Locate the cells, classifying each as a parasitized RBC, an uninfected RBC, or a WBC.
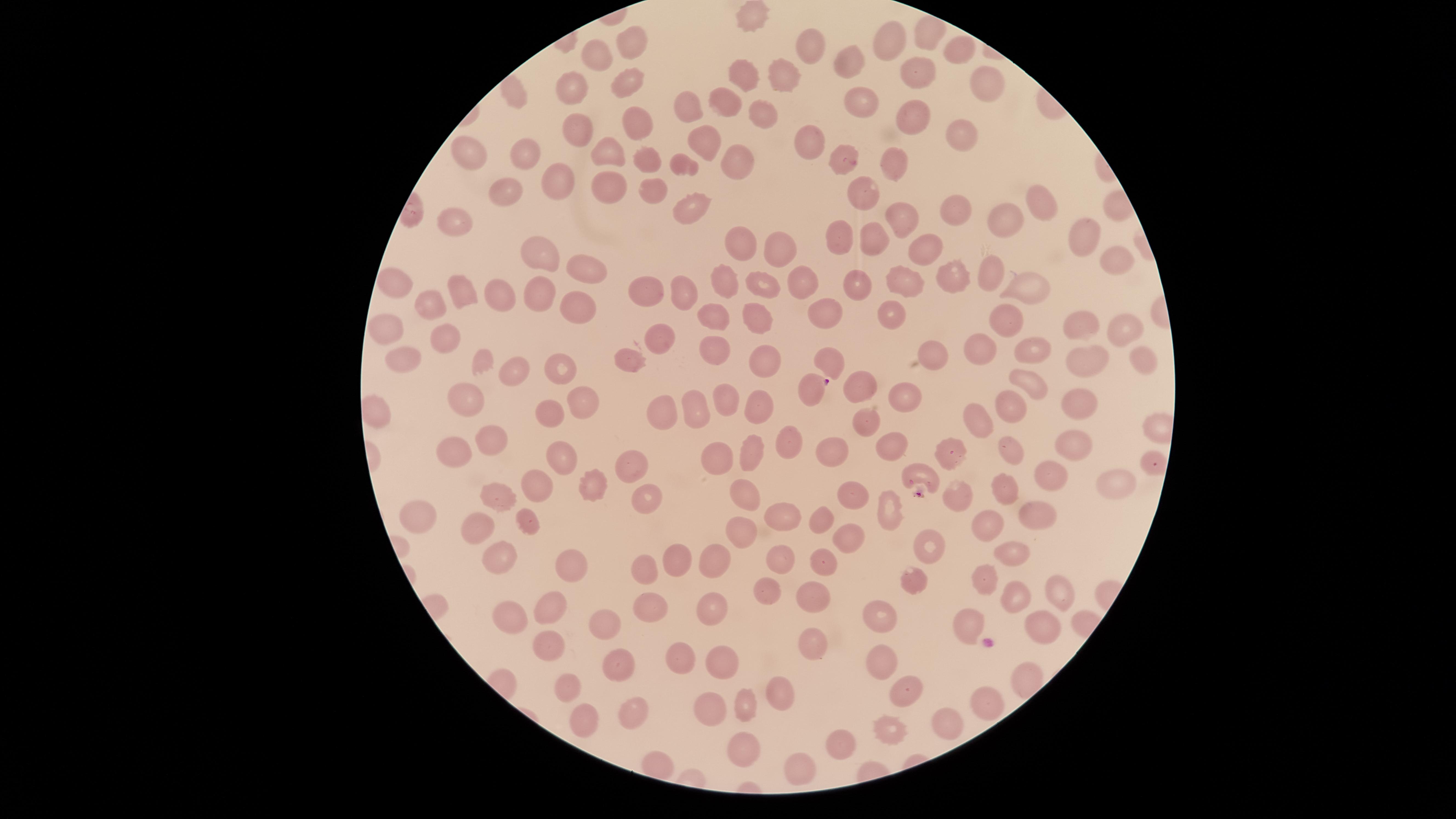
Approximate marker points, in pixels from the top-left corner.
Parasitized RBCs: (x=807, y=392), (x=920, y=477).
Uninfected RBCs: (x=750, y=21), (x=926, y=35), (x=635, y=41), (x=806, y=44), (x=891, y=45), (x=951, y=49), (x=600, y=55), (x=841, y=60), (x=912, y=68), (x=744, y=76), (x=785, y=78), (x=623, y=79), (x=574, y=83), (x=515, y=87), (x=989, y=90), (x=854, y=100), (x=728, y=102), (x=679, y=106), (x=910, y=114), (x=761, y=118), (x=635, y=123), (x=567, y=129), (x=959, y=140), (x=807, y=141), (x=705, y=142), (x=601, y=150), (x=465, y=152), (x=527, y=152), (x=837, y=157), (x=647, y=161), (x=892, y=162), (x=677, y=163), (x=736, y=165), (x=557, y=182), (x=611, y=188), (x=647, y=188), (x=510, y=191), (x=859, y=192), (x=1036, y=201), (x=690, y=208), (x=953, y=209), (x=461, y=220), (x=908, y=220), (x=1001, y=220), (x=1083, y=231), (x=837, y=236), (x=741, y=237), (x=865, y=239), (x=768, y=246), (x=921, y=249), (x=548, y=253), (x=1110, y=260), (x=587, y=265), (x=992, y=274), (x=954, y=278), (x=763, y=280), (x=899, y=282), (x=393, y=283), (x=1020, y=283), (x=802, y=284), (x=728, y=285), (x=864, y=285), (x=653, y=288), (x=460, y=291), (x=502, y=291), (x=683, y=291), (x=543, y=295), (x=427, y=302), (x=576, y=306), (x=825, y=312), (x=882, y=313), (x=712, y=317), (x=756, y=317), (x=1003, y=319), (x=1066, y=324), (x=1126, y=325), (x=379, y=326), (x=668, y=338), (x=443, y=341), (x=715, y=346), (x=975, y=348), (x=933, y=352), (x=828, y=354), (x=1031, y=355), (x=1134, y=357), (x=761, y=359), (x=633, y=360), (x=403, y=361), (x=1084, y=362), (x=516, y=367), (x=565, y=370), (x=854, y=386), (x=1032, y=387), (x=914, y=397), (x=464, y=398), (x=724, y=399), (x=582, y=402), (x=1011, y=405), (x=1080, y=405), (x=665, y=410), (x=757, y=410), (x=696, y=413), (x=551, y=416), (x=976, y=418), (x=862, y=420), (x=490, y=436), (x=784, y=440), (x=1068, y=440), (x=887, y=447), (x=951, y=452), (x=1008, y=452), (x=749, y=454), (x=827, y=454), (x=459, y=455), (x=564, y=459), (x=715, y=459), (x=631, y=463), (x=1152, y=464), (x=1044, y=474), (x=1120, y=479), (x=1000, y=484), (x=589, y=485), (x=539, y=487), (x=500, y=493), (x=646, y=494), (x=742, y=494), (x=855, y=494), (x=956, y=498), (x=894, y=505), (x=1034, y=512), (x=422, y=513), (x=781, y=514), (x=821, y=518), (x=526, y=520), (x=476, y=525), (x=989, y=530), (x=740, y=533), (x=848, y=539), (x=928, y=546), (x=775, y=554), (x=1011, y=554), (x=716, y=555), (x=672, y=556), (x=501, y=558), (x=647, y=562), (x=567, y=563), (x=827, y=563), (x=917, y=576), (x=988, y=583), (x=761, y=587), (x=1054, y=588), (x=812, y=593), (x=1008, y=596), (x=555, y=605), (x=711, y=605), (x=651, y=606), (x=872, y=607), (x=603, y=617), (x=511, y=620), (x=1037, y=628), (x=976, y=630), (x=810, y=640), (x=549, y=641), (x=876, y=656), (x=681, y=658), (x=723, y=660), (x=613, y=667), (x=1028, y=680), (x=569, y=684), (x=904, y=688), (x=772, y=693), (x=987, y=704), (x=741, y=705), (x=708, y=708), (x=626, y=713), (x=582, y=718), (x=888, y=724), (x=944, y=726), (x=839, y=740), (x=752, y=750), (x=799, y=768).
No WBCs identified.

Thin blood film. Photographed with a smartphone camera through the microscope eyepiece. Giemsa-stained preparation. One field of view of the specimen. The visible region is circular. Image is 1456×819 pixels. Species: Plasmodium falciparum.